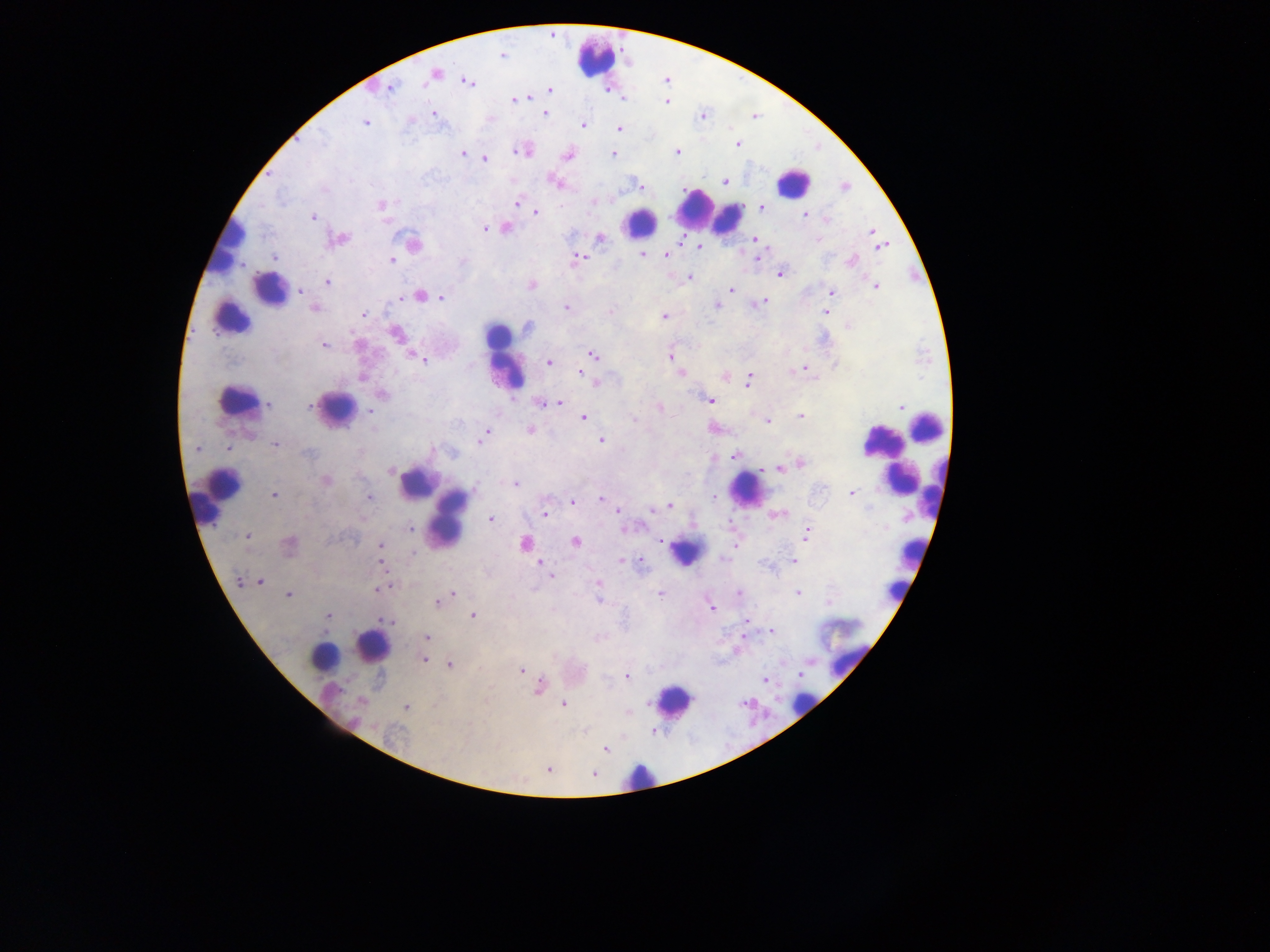

{
  "field_of_view": "single",
  "preparation": "thick blood film",
  "image_size": "1270×952 pixels",
  "capture": "mobile-phone photograph through a microscope",
  "plasmodium_parasite_locations": "approximate centers as x y in pixels: 502 55; 435 73; 468 82; 390 88; 549 89; 528 97; 514 100; 667 101; 545 113; 434 114; 702 116; 365 123; 583 125; 619 129; 321 138; 738 145; 518 151; 677 152; 463 153; 613 154; 568 156; 484 159; 725 181; 555 183; 640 187; 846 187; 324 190; 593 202; 517 203; 381 204; 520 205; 762 208; 536 212; 805 215; 312 217; 825 219; 385 220; 505 228; 485 229; 872 231; 600 237; 340 239; 818 239; 680 240; 755 240; 413 244; 880 245; 699 248; 641 254; 666 255; 757 257; 273 258; 577 258; 392 260; 851 261; 781 274; 689 277; 327 283; 531 286; 875 287; 731 289; 301 291; 831 292; 419 295; 441 297; 762 302; 752 305; 717 306; 566 307; 315 308; 610 311; 826 312; 364 315; 664 317; 848 326; 528 327; 397 334; 324 346; 593 355; 415 356; 669 357; 422 359; 549 363; 805 368; 581 374; 681 374; 362 378; 748 380; 594 382; 382 395; 709 400; 558 403; 269 404; 542 404; 310 405; 900 406; 660 407; 371 411; 801 416; 583 418; 634 419; 767 421; 530 430; 486 433; 482 439; 601 441; 275 445; 197 448; 228 449; 308 453; 735 455; 801 463; 779 469; 390 470; 326 481; 515 484; 850 493; 274 494; 368 497; 714 497; 601 499; 573 501; 670 506; 618 509; 545 513; 775 515; 491 519; 410 529; 807 534; 248 536; 576 541; 662 541; 289 543; 525 543; 734 545; 380 546; 622 561; 794 561; 381 563; 640 563; 540 564; 545 568; 550 576; 239 580; 260 581; 598 584; 377 589; 739 592; 798 592; 452 594; 660 594; 289 595; 599 600; 438 602; 712 608; 328 616; 473 616; 387 621; 746 623; 772 632; 427 637; 743 637; 424 660; 450 665; 521 670; 626 676; 765 679; 539 687; 361 701; 563 704; 405 707; 605 748; 548 769; 594 775",
  "leukocyte_locations": "approximate centers as x y in pixels: 597 59; 793 182; 700 209; 728 217; 640 221; 229 244; 269 290; 230 317; 505 358; 236 399; 337 407; 927 426; 882 440; 890 463; 901 477; 415 484; 746 490; 220 496; 450 517; 686 552; 911 553; 895 590; 372 646; 840 652; 326 657; 673 700; 803 704; 639 776",
  "country": "Ghana"
}